Give the extent of all Plasmodium falciparum-infected red blood cells.
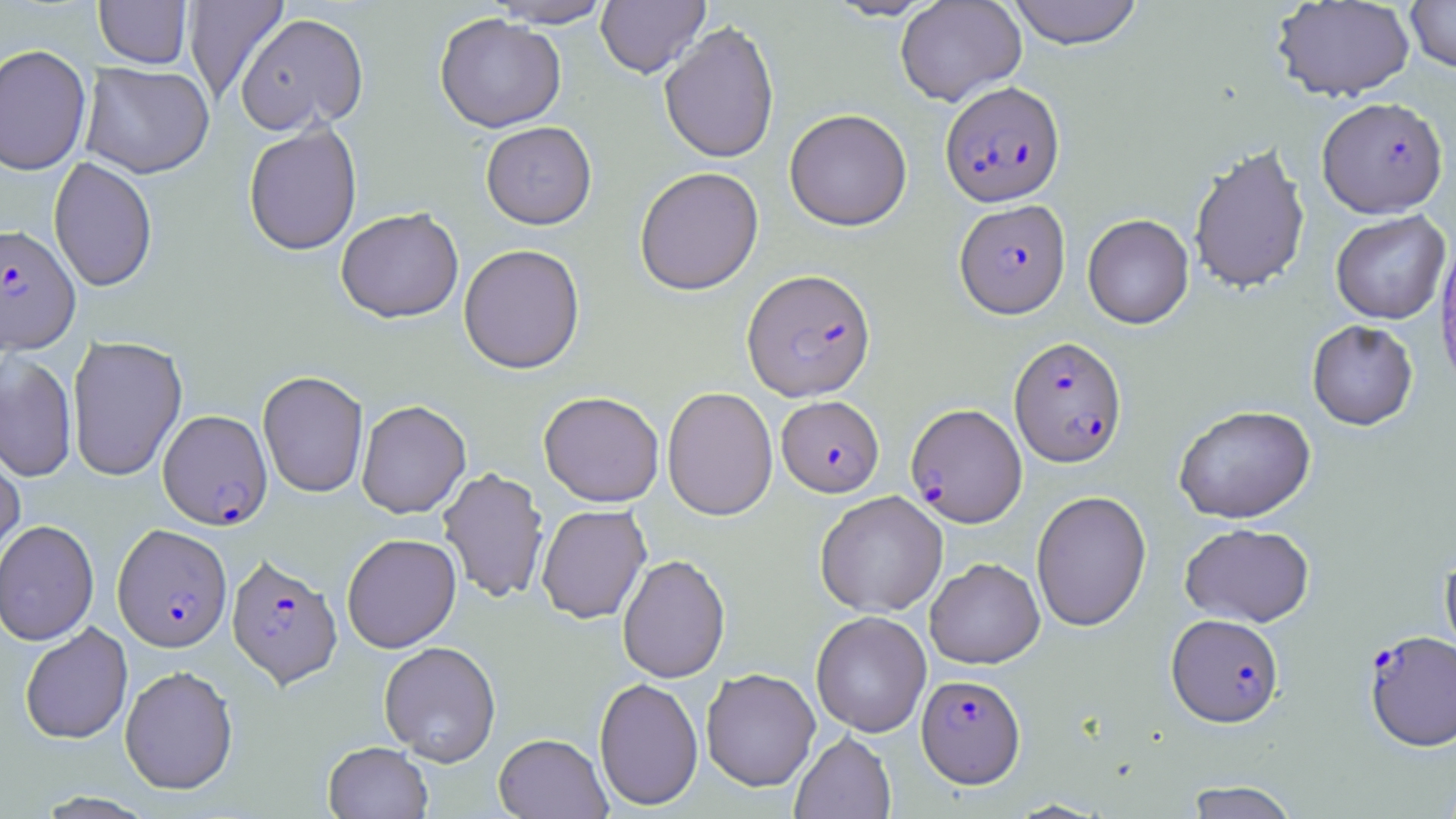

Approximate bounding boxes as named x1/y1/x2/y2 corners in pixels.
Plasmodium falciparum-infected red blood cells: (x1=940, y1=81, x2=1065, y2=207), (x1=1317, y1=97, x2=1448, y2=218), (x1=954, y1=199, x2=1070, y2=319), (x1=0, y1=224, x2=80, y2=354), (x1=742, y1=268, x2=877, y2=401), (x1=1008, y1=336, x2=1127, y2=468), (x1=777, y1=395, x2=884, y2=497), (x1=906, y1=403, x2=1027, y2=527), (x1=158, y1=409, x2=272, y2=530), (x1=113, y1=523, x2=233, y2=652), (x1=226, y1=554, x2=343, y2=690), (x1=1167, y1=613, x2=1285, y2=727), (x1=1365, y1=630, x2=1455, y2=751), (x1=916, y1=673, x2=1025, y2=788).

Summary:
  - Uninfected red blood cell locations: (x1=183, y1=0, x2=289, y2=105), (x1=482, y1=0, x2=615, y2=28), (x1=596, y1=0, x2=710, y2=78), (x1=823, y1=0, x2=942, y2=21), (x1=895, y1=0, x2=1027, y2=106), (x1=1006, y1=0, x2=1145, y2=49), (x1=1404, y1=0, x2=1456, y2=73), (x1=94, y1=1, x2=192, y2=70), (x1=1272, y1=1, x2=1415, y2=102), (x1=235, y1=12, x2=369, y2=136), (x1=435, y1=14, x2=566, y2=133), (x1=659, y1=20, x2=780, y2=164), (x1=0, y1=44, x2=92, y2=176), (x1=81, y1=63, x2=214, y2=179), (x1=784, y1=109, x2=912, y2=231), (x1=243, y1=121, x2=362, y2=256), (x1=481, y1=121, x2=597, y2=231), (x1=1188, y1=142, x2=1311, y2=296), (x1=49, y1=157, x2=158, y2=292), (x1=634, y1=166, x2=764, y2=296), (x1=336, y1=208, x2=464, y2=324), (x1=1330, y1=210, x2=1451, y2=324), (x1=1082, y1=213, x2=1194, y2=329), (x1=458, y1=244, x2=585, y2=375), (x1=1307, y1=320, x2=1418, y2=430), (x1=67, y1=335, x2=187, y2=481), (x1=0, y1=351, x2=77, y2=482), (x1=258, y1=371, x2=369, y2=498), (x1=662, y1=386, x2=778, y2=521), (x1=539, y1=391, x2=664, y2=506), (x1=356, y1=400, x2=471, y2=519), (x1=1174, y1=404, x2=1316, y2=523), (x1=0, y1=442, x2=25, y2=576), (x1=438, y1=467, x2=549, y2=604), (x1=815, y1=490, x2=948, y2=617), (x1=1031, y1=490, x2=1151, y2=631), (x1=536, y1=504, x2=651, y2=624), (x1=0, y1=519, x2=99, y2=645), (x1=1179, y1=522, x2=1315, y2=627), (x1=341, y1=533, x2=462, y2=653), (x1=1439, y1=548, x2=1456, y2=666), (x1=617, y1=554, x2=730, y2=683), (x1=925, y1=557, x2=1045, y2=669), (x1=810, y1=610, x2=932, y2=737), (x1=20, y1=623, x2=133, y2=745), (x1=379, y1=641, x2=501, y2=766), (x1=119, y1=665, x2=238, y2=795), (x1=700, y1=667, x2=821, y2=791), (x1=593, y1=676, x2=704, y2=811), (x1=790, y1=730, x2=896, y2=819), (x1=494, y1=733, x2=611, y2=819), (x1=323, y1=741, x2=433, y2=818), (x1=1183, y1=781, x2=1300, y2=819)
  - Slide-level diagnosis: Plasmodium falciparum
  - Modality: optical microscopy
  - Stain: May-Grünwald-Giemsa
  - Magnification: 1000x
  - Field of view: single
  - Preparation: thin blood smear
  - Image size: 1456×819 pixels